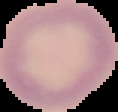

The area outside the segmented cell region is set to black. Malaria status: uninfected. Image is 118×112 pixels. From a thin blood smear.